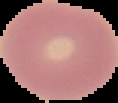
Summary:
  - Image size: 118×103 pixels
  - Image type: segmented cell region with the area outside set to black
  - Result: no malaria parasites detected
  - Preparation: thin blood smear